Classify this cell by malaria status.
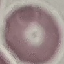
It is uninfected.

image_type: automatically extracted cell patch, resized to 64 × 64 pixels
capture: smartphone camera at the microscope eyepiece
preparation: thin blood smear
stain: Giemsa